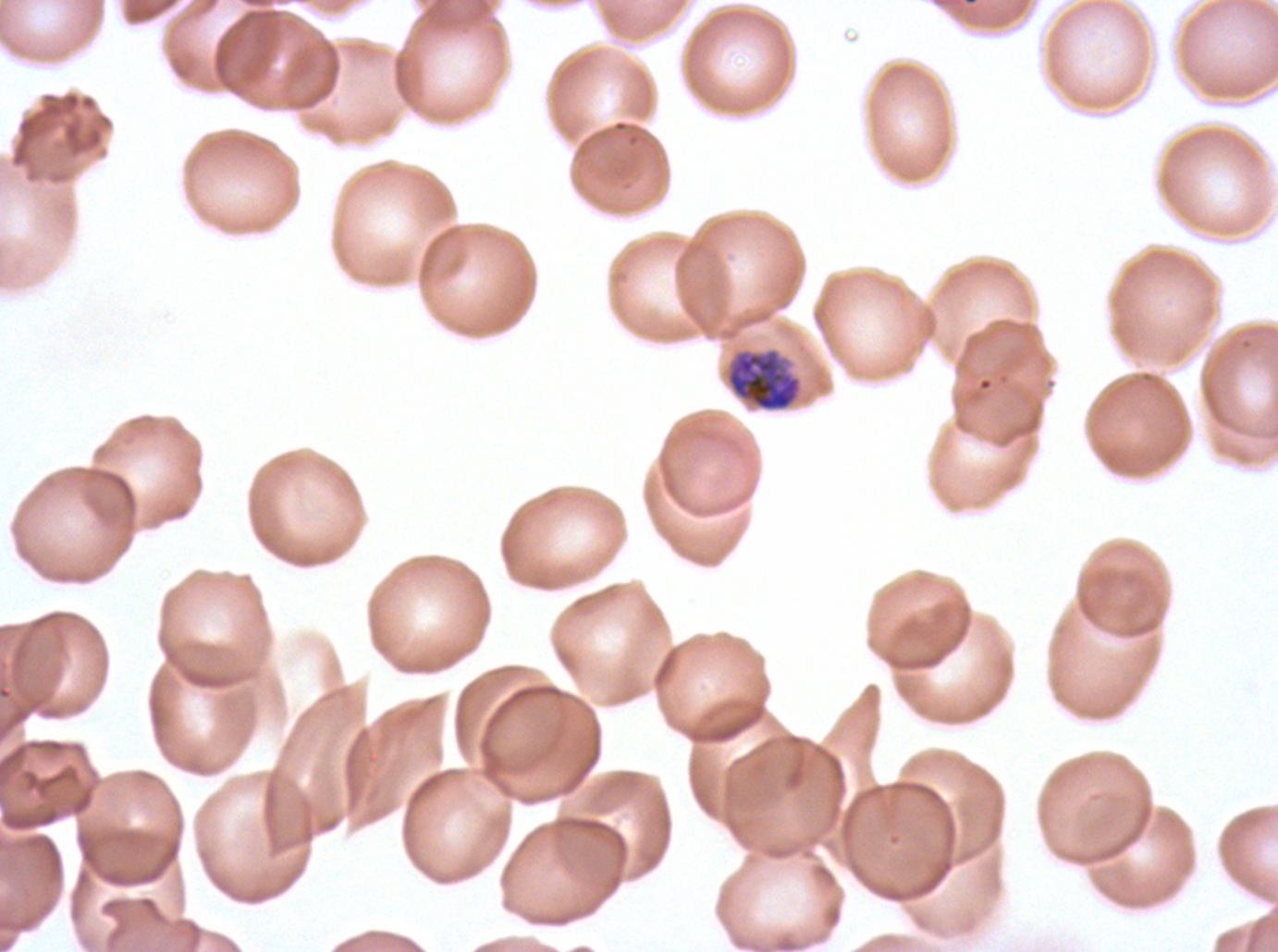

Approximate bounding boxes as (x1, y1, x2, y2) in pixels. Early schizont locations: (725, 347, 803, 412). Giemsa-stained preparation. Plasmodium falciparum cultured ex vivo for 24 to 48 hours, from a patient in The Gambia. Thin blood smear. One sub-image of a larger composite. Image is 1278×952 pixels.